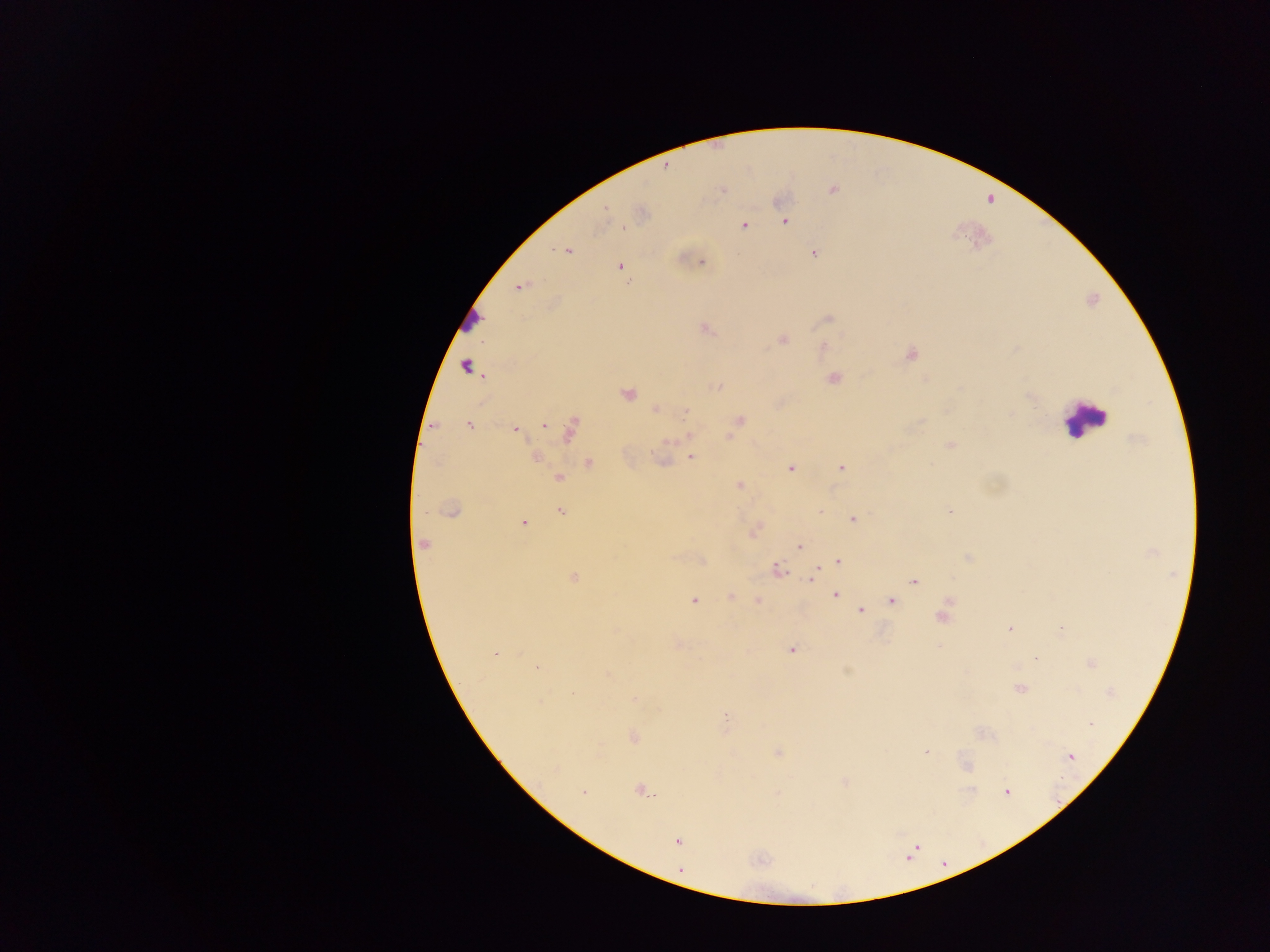
Approximate centers as (x, y) in pixels. Leukocyte locations: (468, 320), (1084, 419). Malaria parasite locations: (666, 167), (723, 190), (832, 190), (606, 208), (785, 222), (744, 225), (624, 227), (568, 251), (814, 254), (701, 262), (620, 267), (520, 286), (828, 318), (707, 328), (782, 340), (823, 346), (910, 355), (465, 366), (834, 379), (717, 386), (628, 393), (1029, 397), (656, 409), (685, 412), (740, 420), (469, 426), (544, 426), (515, 429), (569, 429), (688, 436), (728, 437), (949, 445), (653, 455), (536, 457), (690, 457), (589, 463), (841, 467), (791, 469), (559, 479), (739, 485), (452, 510), (424, 511), (560, 511), (949, 511), (853, 519), (524, 523), (423, 544), (800, 546), (969, 557), (838, 561), (777, 569), (574, 577), (812, 579), (915, 581), (835, 595), (731, 596), (758, 600), (693, 601), (891, 601), (860, 610), (942, 617), (1009, 628), (1061, 628), (792, 650), (495, 653), (1035, 659), (537, 667), (608, 674), (1019, 689), (634, 699), (726, 716), (1090, 723), (633, 737), (926, 752), (778, 753), (1070, 756), (641, 791), (1007, 791), (582, 793), (677, 841). Image is 1270×952 pixels. Photographed through a microscope with a mobile-phone camera. One field of view. Thick blood film. Collected in Ghana.